State the preparation type.
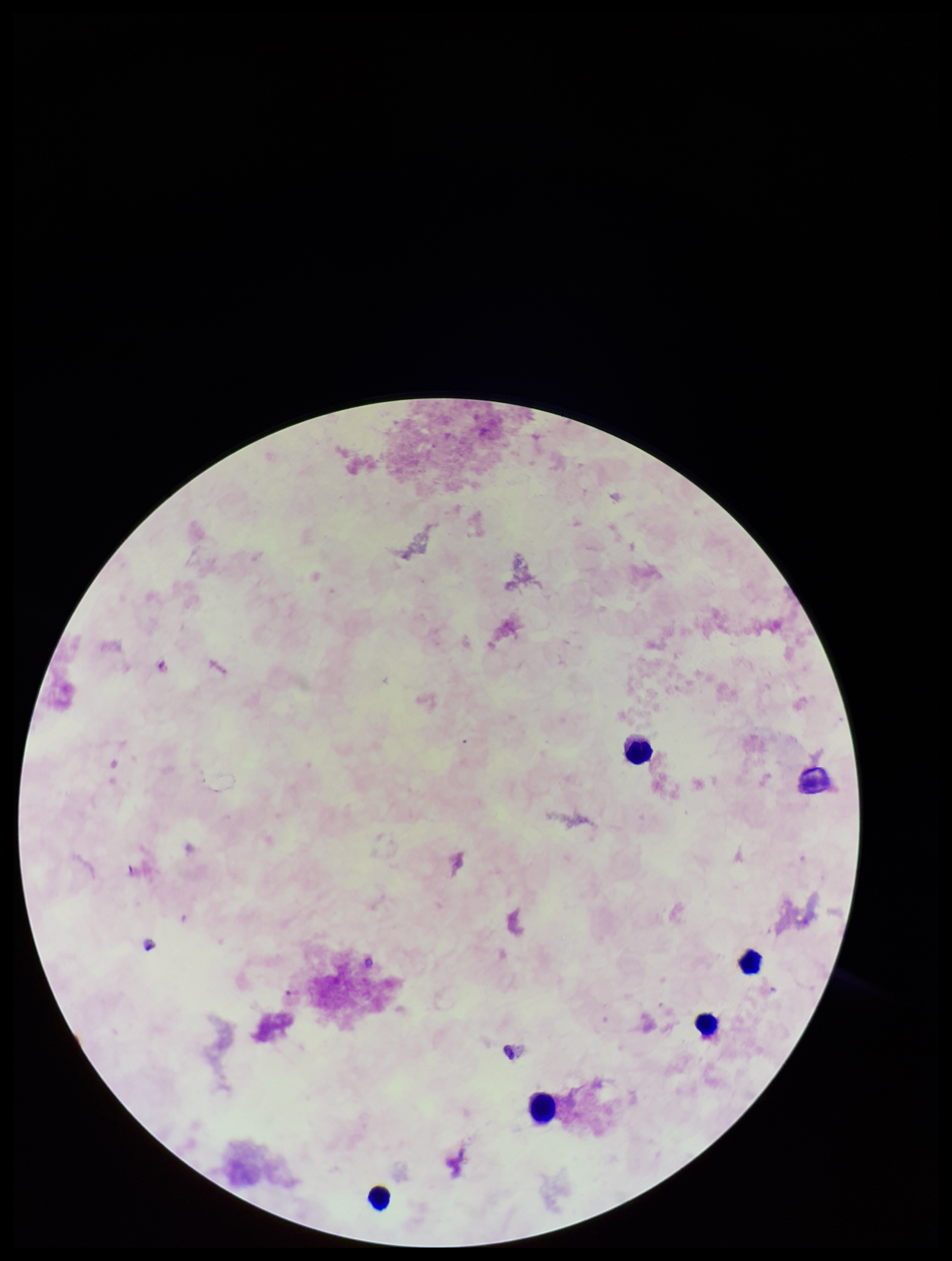

Thick.

capture: smartphone photograph through the microscope eyepiece
field_of_view: single
patient_malaria_status: negative
plasmodium_parasites: none identified
leukocyte_count: 5
parasite_count: 0
stain: Giemsa
image_size: 952×1261 pixels